Give the extent of all Plasmodium ovale-infected red blood cells.
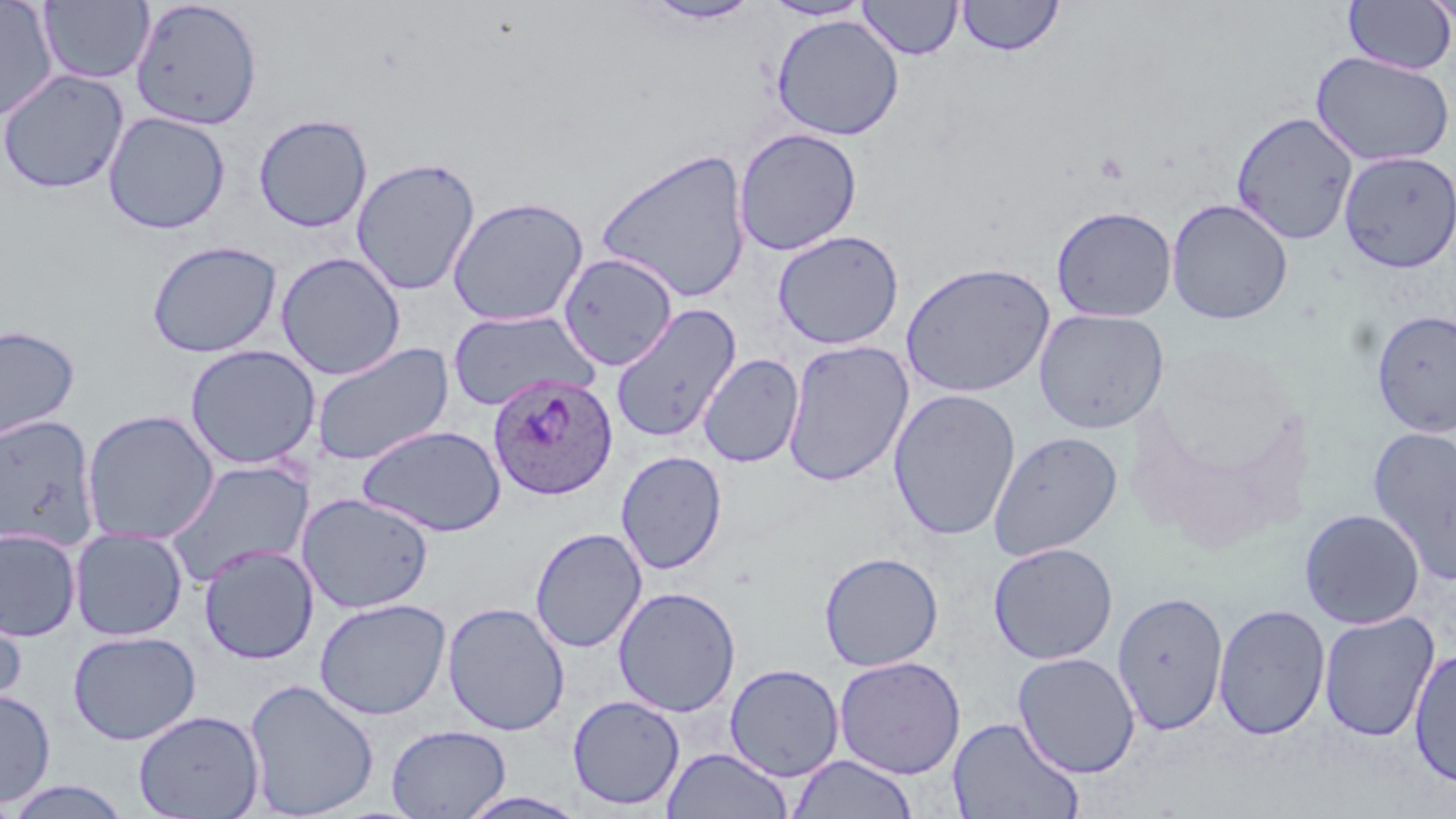
Approximate bounding boxes as (x1,y1)-(x2,y2) corner pairs in pixels.
Plasmodium ovale-infected red blood cells: (487,372)-(618,501).

Summary:
  - Uninfected red blood cell locations: (0,0)-(59,121), (857,0)-(963,60), (956,0)-(1063,56), (1421,0)-(1456,29), (38,1)-(154,84), (129,1)-(263,130), (643,1)-(761,25), (762,1)-(873,21), (1342,1)-(1456,75), (770,14)-(905,140), (1311,51)-(1455,166), (0,68)-(129,195), (102,111)-(231,235), (1230,111)-(1358,245), (253,114)-(372,232), (733,127)-(863,256), (595,148)-(753,303), (1337,150)-(1455,273), (351,157)-(480,296), (446,196)-(589,327), (1166,198)-(1293,325), (1051,205)-(1177,322), (772,229)-(905,350), (147,239)-(283,358), (276,252)-(405,380), (557,253)-(677,370), (900,261)-(1055,398), (610,303)-(742,444), (448,308)-(600,412), (1033,308)-(1170,433), (1371,308)-(1456,436), (0,324)-(80,446), (782,339)-(914,487), (310,341)-(454,467), (184,344)-(321,470), (698,353)-(803,468), (888,388)-(1021,542), (81,409)-(220,545), (0,414)-(100,553), (357,424)-(506,537), (1367,426)-(1456,586), (987,431)-(1123,561), (616,450)-(727,575), (163,459)-(314,588), (297,493)-(435,614), (1299,508)-(1425,629), (69,527)-(189,640), (529,527)-(647,653), (0,528)-(82,641), (988,542)-(1119,665), (198,543)-(319,664), (818,551)-(943,671), (613,586)-(741,717), (1112,590)-(1229,737), (0,595)-(26,716), (314,598)-(451,720), (442,601)-(570,736), (1213,603)-(1330,740), (1318,611)-(1440,742), (68,629)-(201,745), (1408,648)-(1456,788), (1012,652)-(1141,777), (833,656)-(965,779), (724,663)-(845,782), (244,678)-(380,818), (0,688)-(55,807), (567,694)-(685,810), (133,710)-(265,818), (947,717)-(1085,819), (386,724)-(510,819), (662,747)-(792,819), (787,753)-(918,818), (6,779)-(132,819), (456,791)-(591,819)
  - Slide-level diagnosis: Plasmodium ovale
  - Image size: 1456×819 pixels
  - Preparation: thin blood film
  - Magnification: 1000x
  - Modality: optical microscopy
  - Stain: May-Grünwald-Giemsa
  - Field of view: single